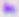
Summary:
  - Magnification: 400x
  - Identification: Toxoplasma gondii
  - Modality: photomicrograph